Identify the blood parasite species.
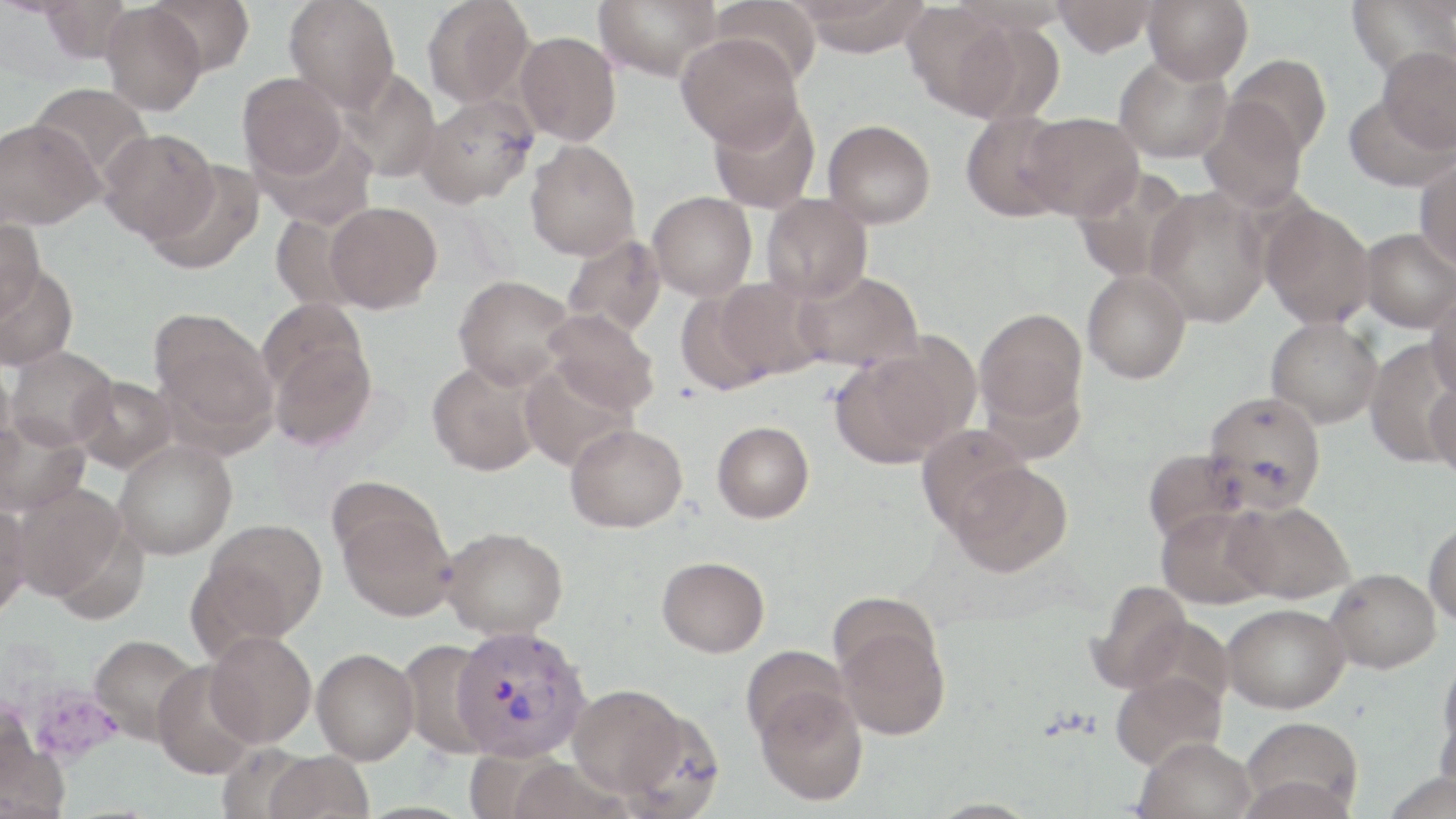

Plasmodium vivax.

Summary:
  - Coordinate format: approximate bounding boxes as named x1/y1/x2/y2 corners in pixels
  - Uninfected red blood cell locations: (x1=147, y1=0, x2=254, y2=77), (x1=284, y1=0, x2=400, y2=111), (x1=422, y1=0, x2=535, y2=108), (x1=594, y1=0, x2=721, y2=81), (x1=710, y1=0, x2=822, y2=86), (x1=793, y1=0, x2=933, y2=56), (x1=1051, y1=0, x2=1157, y2=57), (x1=1142, y1=0, x2=1253, y2=84), (x1=1347, y1=0, x2=1455, y2=80), (x1=36, y1=1, x2=133, y2=63), (x1=100, y1=3, x2=206, y2=116), (x1=902, y1=4, x2=1022, y2=119), (x1=514, y1=31, x2=621, y2=145), (x1=676, y1=32, x2=803, y2=150), (x1=1378, y1=47, x2=1456, y2=155), (x1=1114, y1=54, x2=1232, y2=163), (x1=1225, y1=54, x2=1332, y2=158), (x1=340, y1=69, x2=442, y2=183), (x1=237, y1=72, x2=347, y2=182), (x1=28, y1=82, x2=152, y2=185), (x1=1343, y1=91, x2=1453, y2=194), (x1=419, y1=94, x2=538, y2=207), (x1=708, y1=98, x2=820, y2=213), (x1=1199, y1=99, x2=1308, y2=211), (x1=959, y1=109, x2=1076, y2=222), (x1=1023, y1=112, x2=1143, y2=221), (x1=0, y1=117, x2=103, y2=230), (x1=823, y1=119, x2=936, y2=229), (x1=99, y1=128, x2=218, y2=242), (x1=525, y1=140, x2=640, y2=260), (x1=1414, y1=158, x2=1456, y2=270), (x1=147, y1=160, x2=265, y2=275), (x1=1073, y1=168, x2=1193, y2=284), (x1=1144, y1=187, x2=1272, y2=327), (x1=647, y1=191, x2=757, y2=301), (x1=762, y1=193, x2=872, y2=304), (x1=324, y1=201, x2=442, y2=313), (x1=1259, y1=203, x2=1375, y2=329), (x1=268, y1=212, x2=365, y2=313), (x1=0, y1=217, x2=45, y2=319), (x1=1360, y1=228, x2=1456, y2=333), (x1=562, y1=235, x2=667, y2=338), (x1=0, y1=262, x2=78, y2=372), (x1=793, y1=269, x2=923, y2=372), (x1=1082, y1=269, x2=1191, y2=384), (x1=453, y1=274, x2=575, y2=390), (x1=713, y1=277, x2=828, y2=382), (x1=673, y1=285, x2=782, y2=396), (x1=1426, y1=289, x2=1456, y2=402), (x1=542, y1=308, x2=659, y2=415), (x1=975, y1=308, x2=1087, y2=429), (x1=150, y1=309, x2=277, y2=441), (x1=1266, y1=317, x2=1383, y2=428), (x1=265, y1=328, x2=377, y2=452), (x1=1364, y1=339, x2=1454, y2=468), (x1=831, y1=343, x2=968, y2=469), (x1=5, y1=346, x2=118, y2=451), (x1=0, y1=360, x2=17, y2=471), (x1=427, y1=360, x2=542, y2=476), (x1=518, y1=361, x2=637, y2=472), (x1=72, y1=374, x2=177, y2=473), (x1=1427, y1=379, x2=1456, y2=484), (x1=1203, y1=390, x2=1326, y2=513), (x1=0, y1=416, x2=90, y2=516), (x1=712, y1=420, x2=814, y2=523), (x1=565, y1=423, x2=687, y2=533), (x1=917, y1=426, x2=1031, y2=535), (x1=114, y1=440, x2=237, y2=560), (x1=1142, y1=449, x2=1247, y2=547), (x1=947, y1=459, x2=1073, y2=578), (x1=12, y1=483, x2=128, y2=604), (x1=335, y1=497, x2=458, y2=622), (x1=0, y1=500, x2=31, y2=619), (x1=1225, y1=500, x2=1354, y2=604), (x1=1156, y1=504, x2=1276, y2=609), (x1=198, y1=518, x2=328, y2=643), (x1=1424, y1=519, x2=1456, y2=627), (x1=442, y1=526, x2=568, y2=639), (x1=657, y1=556, x2=770, y2=658), (x1=1325, y1=567, x2=1441, y2=672), (x1=1087, y1=579, x2=1192, y2=694), (x1=1222, y1=602, x2=1350, y2=713), (x1=834, y1=614, x2=951, y2=741), (x1=205, y1=631, x2=316, y2=748), (x1=88, y1=634, x2=201, y2=744), (x1=398, y1=637, x2=502, y2=759), (x1=741, y1=645, x2=851, y2=746), (x1=1438, y1=647, x2=1456, y2=763), (x1=311, y1=648, x2=419, y2=764), (x1=151, y1=663, x2=258, y2=779), (x1=1111, y1=669, x2=1227, y2=771), (x1=567, y1=684, x2=692, y2=798), (x1=755, y1=685, x2=869, y2=806), (x1=1241, y1=717, x2=1364, y2=816), (x1=1135, y1=737, x2=1257, y2=819), (x1=262, y1=750, x2=375, y2=819)
  - Plasmodium vivax-infected red blood cell locations: (x1=453, y1=623, x2=590, y2=763)
  - Modality: optical microscopy
  - Stain: May-Grünwald-Giemsa
  - Preparation: thin blood smear
  - Magnification: 1000x
  - Field of view: single
  - Image size: 1456×819 pixels